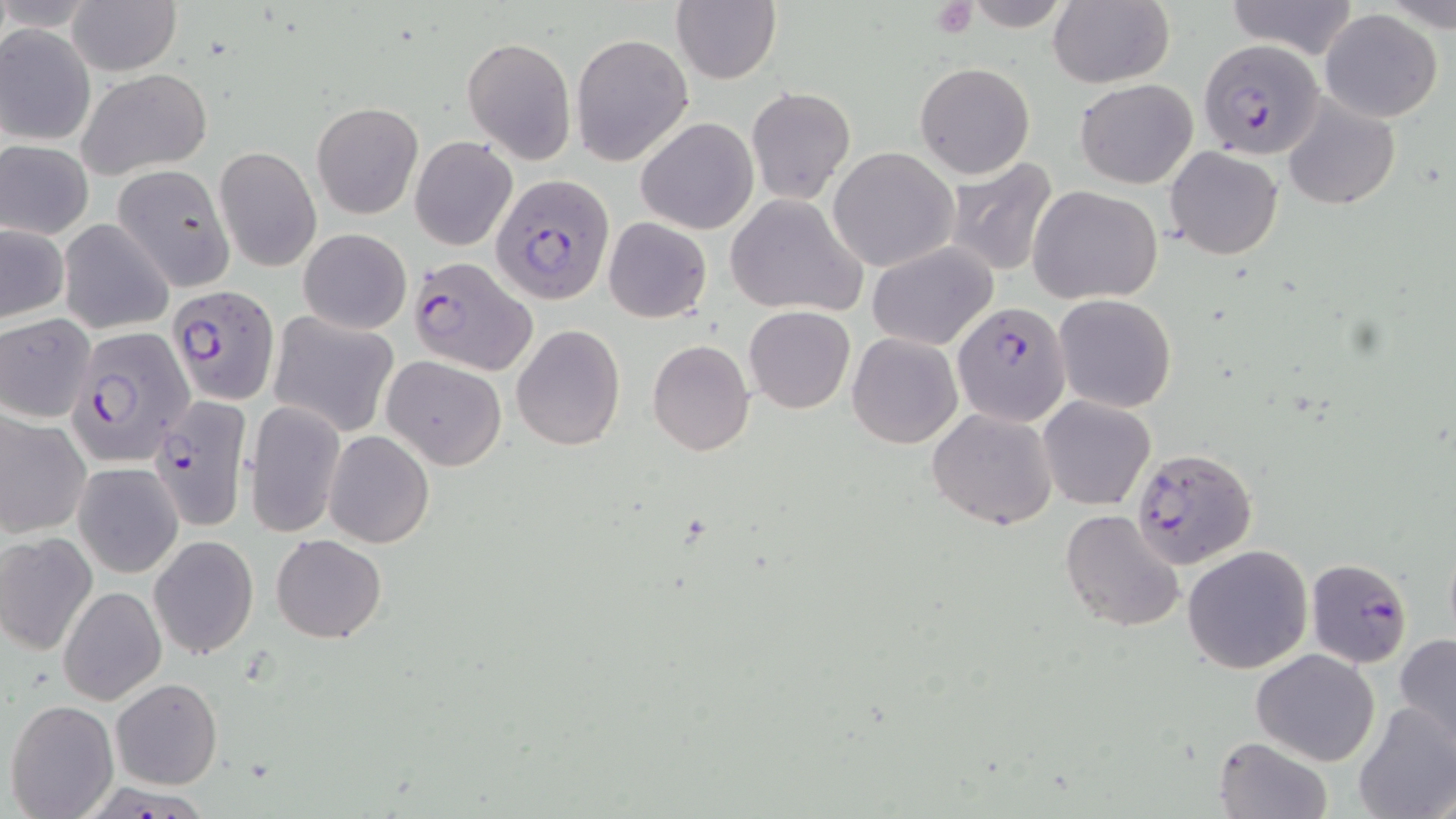
Summary:
  - Coordinate format: approximate bounding boxes as named x1/y1/x2/y2 corners in pixels
  - Uninfected red blood cell locations: (x1=66, y1=0, x2=181, y2=74), (x1=670, y1=0, x2=780, y2=85), (x1=1225, y1=0, x2=1361, y2=59), (x1=1047, y1=1, x2=1174, y2=88), (x1=1319, y1=10, x2=1444, y2=122), (x1=0, y1=24, x2=94, y2=146), (x1=570, y1=33, x2=694, y2=166), (x1=461, y1=35, x2=576, y2=163), (x1=915, y1=62, x2=1036, y2=179), (x1=75, y1=68, x2=213, y2=179), (x1=1074, y1=78, x2=1199, y2=187), (x1=746, y1=86, x2=856, y2=205), (x1=1282, y1=98, x2=1400, y2=209), (x1=312, y1=101, x2=423, y2=219), (x1=636, y1=117, x2=759, y2=234), (x1=410, y1=136, x2=517, y2=250), (x1=1, y1=141, x2=94, y2=239), (x1=214, y1=146, x2=321, y2=273), (x1=1165, y1=146, x2=1284, y2=260), (x1=829, y1=147, x2=957, y2=273), (x1=944, y1=158, x2=1061, y2=278), (x1=114, y1=165, x2=235, y2=291), (x1=1026, y1=184, x2=1163, y2=305), (x1=725, y1=193, x2=869, y2=317), (x1=58, y1=217, x2=174, y2=335), (x1=603, y1=217, x2=712, y2=323), (x1=1, y1=224, x2=69, y2=321), (x1=298, y1=228, x2=412, y2=334), (x1=867, y1=245, x2=998, y2=352), (x1=1053, y1=294, x2=1177, y2=412), (x1=743, y1=305, x2=855, y2=414), (x1=270, y1=312, x2=398, y2=436), (x1=0, y1=314, x2=96, y2=424), (x1=512, y1=325, x2=625, y2=449), (x1=847, y1=332, x2=963, y2=448), (x1=646, y1=338, x2=756, y2=456), (x1=382, y1=356, x2=507, y2=471), (x1=353, y1=375, x2=482, y2=513), (x1=1038, y1=395, x2=1155, y2=511), (x1=244, y1=398, x2=346, y2=539), (x1=926, y1=408, x2=1058, y2=530), (x1=0, y1=410, x2=91, y2=537), (x1=324, y1=430, x2=434, y2=548), (x1=73, y1=462, x2=183, y2=578), (x1=1059, y1=508, x2=1185, y2=632), (x1=0, y1=532, x2=98, y2=656), (x1=271, y1=534, x2=387, y2=643), (x1=150, y1=535, x2=258, y2=659), (x1=1182, y1=544, x2=1313, y2=674), (x1=59, y1=585, x2=166, y2=706), (x1=1394, y1=632, x2=1456, y2=752), (x1=1251, y1=648, x2=1381, y2=766), (x1=110, y1=678, x2=223, y2=789), (x1=6, y1=698, x2=119, y2=818), (x1=1353, y1=701, x2=1456, y2=819), (x1=1213, y1=736, x2=1334, y2=819)
  - Plasmodium falciparum-infected red blood cell locations: (x1=1198, y1=39, x2=1323, y2=160), (x1=490, y1=174, x2=616, y2=305), (x1=408, y1=254, x2=537, y2=375), (x1=169, y1=285, x2=278, y2=403), (x1=951, y1=302, x2=1071, y2=428), (x1=68, y1=326, x2=194, y2=465), (x1=150, y1=393, x2=252, y2=531), (x1=1132, y1=446, x2=1258, y2=570), (x1=1307, y1=559, x2=1413, y2=669), (x1=99, y1=776, x2=216, y2=819)
  - Platelet locations: (x1=932, y1=1, x2=977, y2=39)
  - Slide-level diagnosis: Plasmodium falciparum
  - Field of view: one of a larger specimen
  - Stain: May-Grünwald-Giemsa
  - Image size: 1456×819 pixels
  - Modality: optical microscopy
  - Magnification: 1000x
  - Preparation: thin blood smear